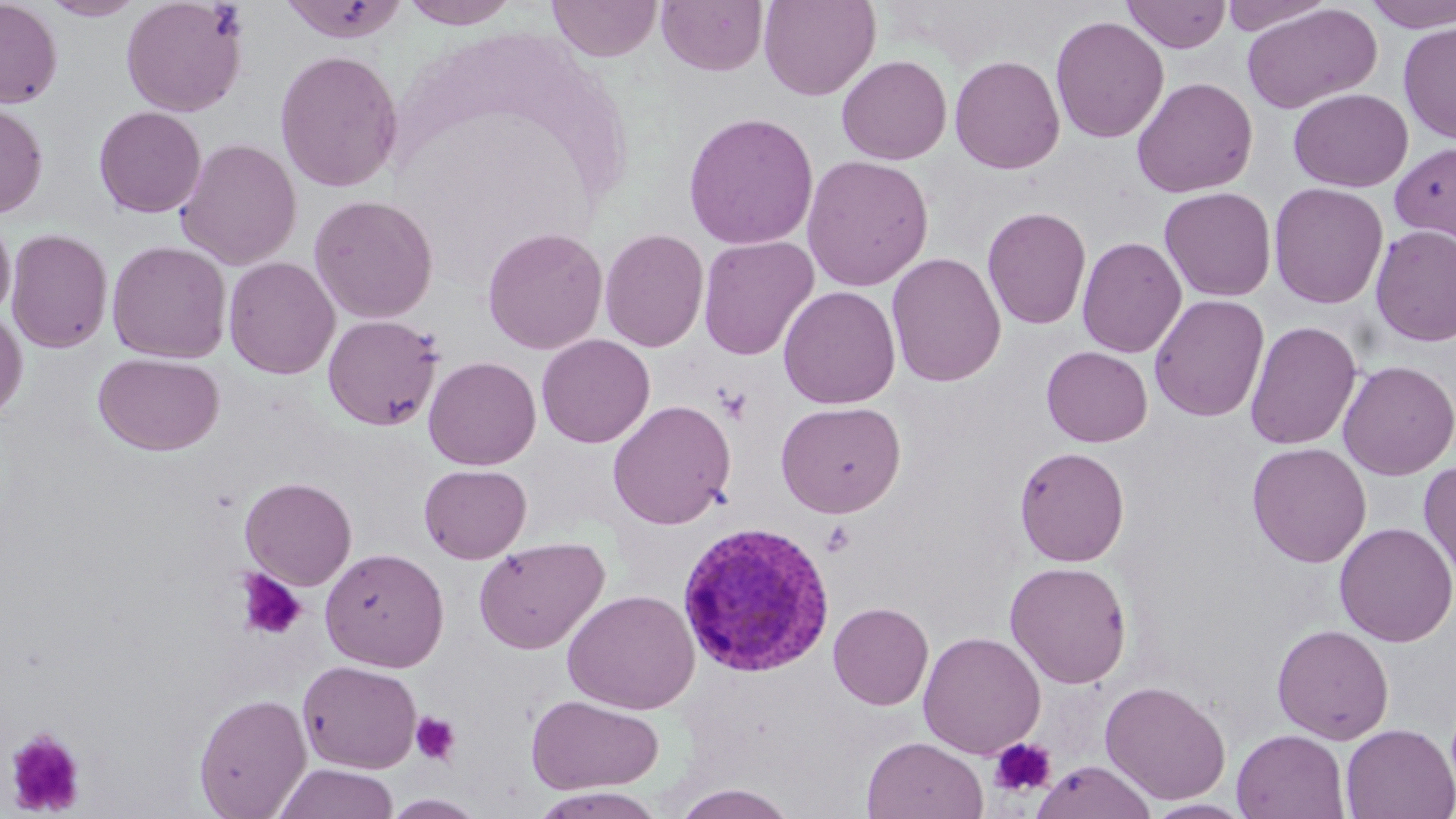
{
  "slide_level_diagnosis": "Plasmodium vivax",
  "modality": "optical microscopy",
  "image_size": "1456×819 pixels",
  "stain": "May-Grünwald-Giemsa",
  "magnification": "1000x",
  "field_of_view": "single",
  "uninfected_red_blood_cell_locations": "approximate bounding boxes as (x1,y1)-(x2,y2) corner pairs in pixels: (0,0)-(62,108), (40,0)-(146,21), (120,0)-(249,117), (279,0)-(410,43), (399,0)-(521,28), (547,0)-(662,61), (657,0)-(768,76), (759,0)-(880,101), (1122,0)-(1231,52), (1221,0)-(1335,35), (1361,1)-(1456,32), (1241,3)-(1382,114), (1049,15)-(1168,144), (1398,22)-(1456,143), (274,49)-(403,192), (836,55)-(952,164), (949,55)-(1065,174), (1131,76)-(1258,197), (1288,88)-(1413,192), (0,100)-(48,220), (93,106)-(207,218), (682,111)-(819,250), (175,137)-(302,270), (1390,142)-(1456,246), (801,154)-(934,292), (1268,182)-(1389,308), (1158,186)-(1277,302), (308,194)-(438,324), (982,206)-(1091,330), (0,210)-(16,322), (1370,225)-(1456,347), (482,226)-(608,354), (5,227)-(114,354), (599,229)-(709,353), (1077,235)-(1187,358), (697,236)-(819,360), (106,240)-(232,363), (885,251)-(1007,387), (223,256)-(340,379), (778,285)-(901,409), (1149,293)-(1270,422), (0,308)-(28,424), (322,314)-(444,431), (1245,320)-(1362,451), (536,334)-(655,448), (1041,345)-(1152,447), (93,352)-(225,456), (423,356)-(541,470), (1338,360)-(1456,480), (607,400)-(736,529), (775,400)-(906,518), (1246,442)-(1371,567), (1014,445)-(1130,566), (1419,460)-(1456,587), (419,464)-(532,563), (240,476)-(357,590), (1334,521)-(1456,647), (473,536)-(610,654), (320,547)-(449,671), (1005,560)-(1132,689), (562,589)-(700,714), (828,602)-(933,710), (1271,623)-(1394,744), (918,631)-(1046,759), (298,660)-(422,773), (1099,680)-(1231,804), (193,693)-(312,818), (526,693)-(665,795), (1340,723)-(1456,819), (1232,728)-(1350,819), (861,735)-(988,819), (1032,760)-(1156,819), (273,763)-(399,819), (671,783)-(798,818), (528,788)-(669,818), (1143,799)-(1254,818)",
  "preparation": "thin blood film",
  "plasmodium_vivax_infected_red_blood_cell_locations": "approximate bounding boxes as (x1,y1)-(x2,y2) corner pairs in pixels: (675,519)-(834,677)",
  "platelet_locations": "approximate bounding boxes as (x1,y1)-(x2,y2) corner pairs in pixels: (716,386)-(753,424), (820,520)-(856,556), (236,569)-(308,642), (411,711)-(461,765), (5,728)-(87,816), (988,737)-(1056,799)"
}